Assess this cell for malaria.
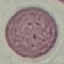

Uninfected.

image type = cell patch, automatically extracted from a larger field of view and resized to 64 × 64 pixels
stain = Giemsa
capture = smartphone camera at the microscope eyepiece
preparation = thin blood smear